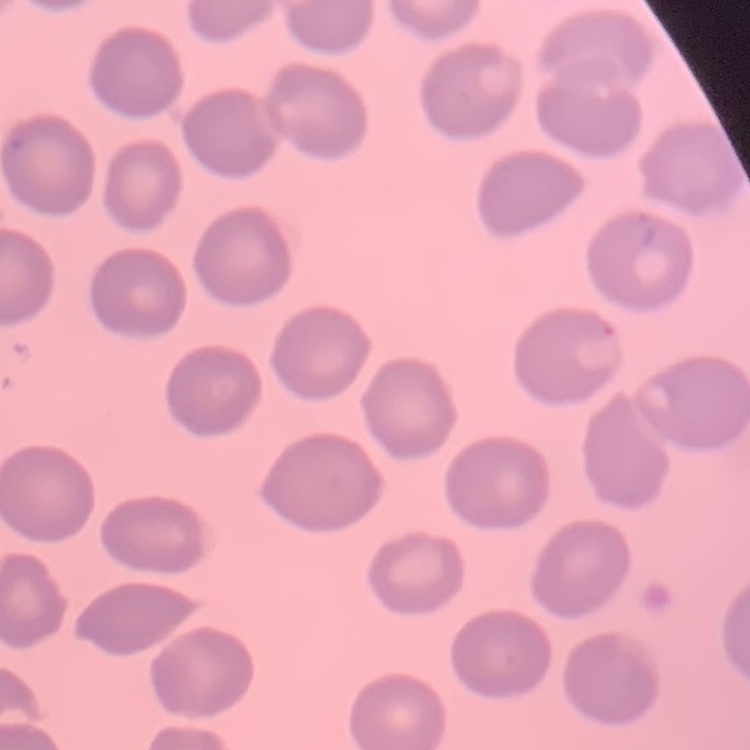 The erythrocytes show no rouleaux formation. Thin blood film. Square crop of a larger photomicrograph. Stained with either Field's or Giemsa.